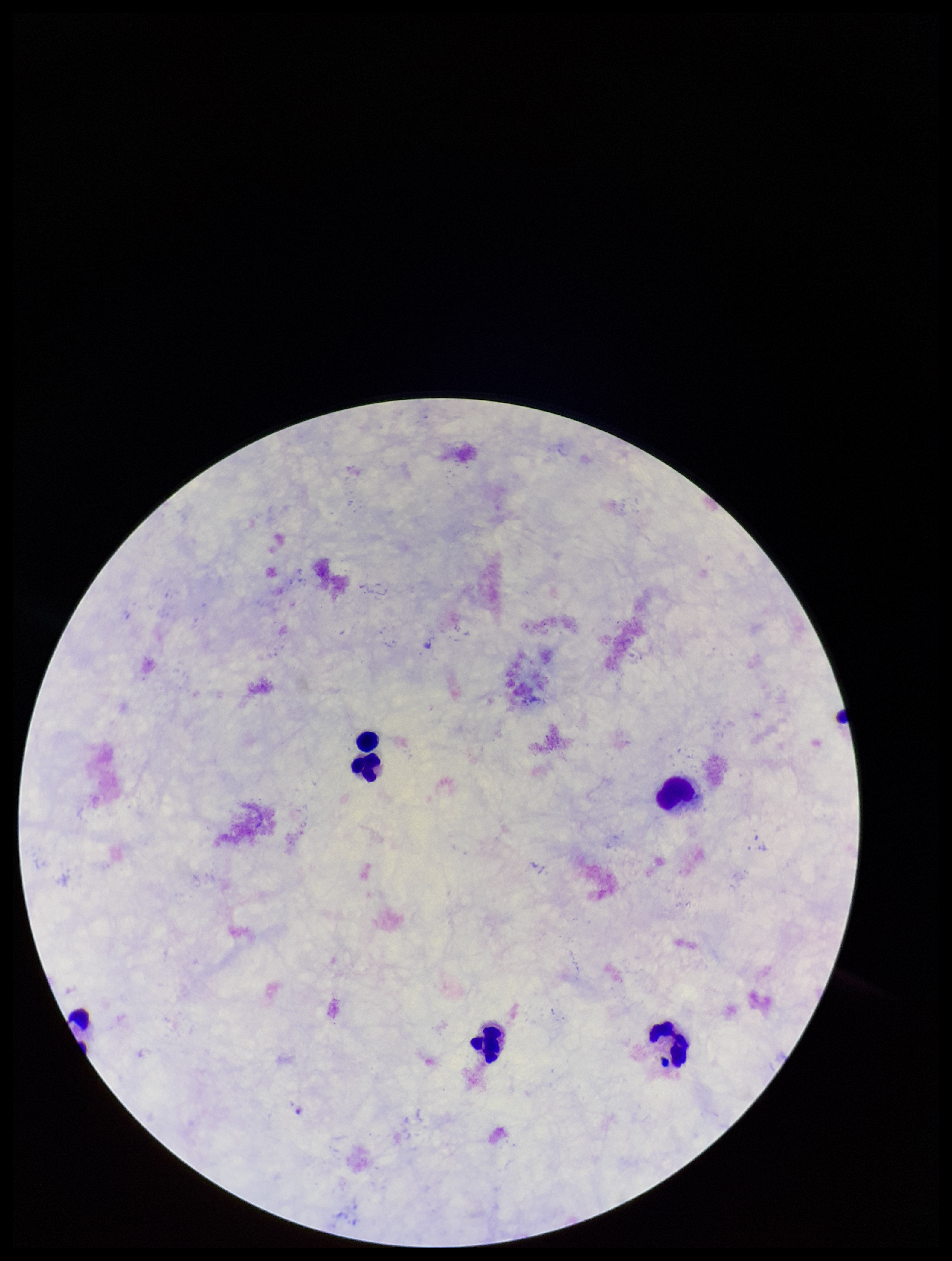
Parasite count: 0. Image is 952×1261 pixels. Plasmodium parasites: none detected. Preparation: thick. Patient malaria status: negative. One field from this slide. Stained with Giemsa. Photographed through the microscope eyepiece with a smartphone camera. Leukocyte count: 6.